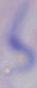

A trypanosome is shown. 1000x magnification. Micrograph.